Give the extent of all Plasmodium falciparum-infected red blood cells.
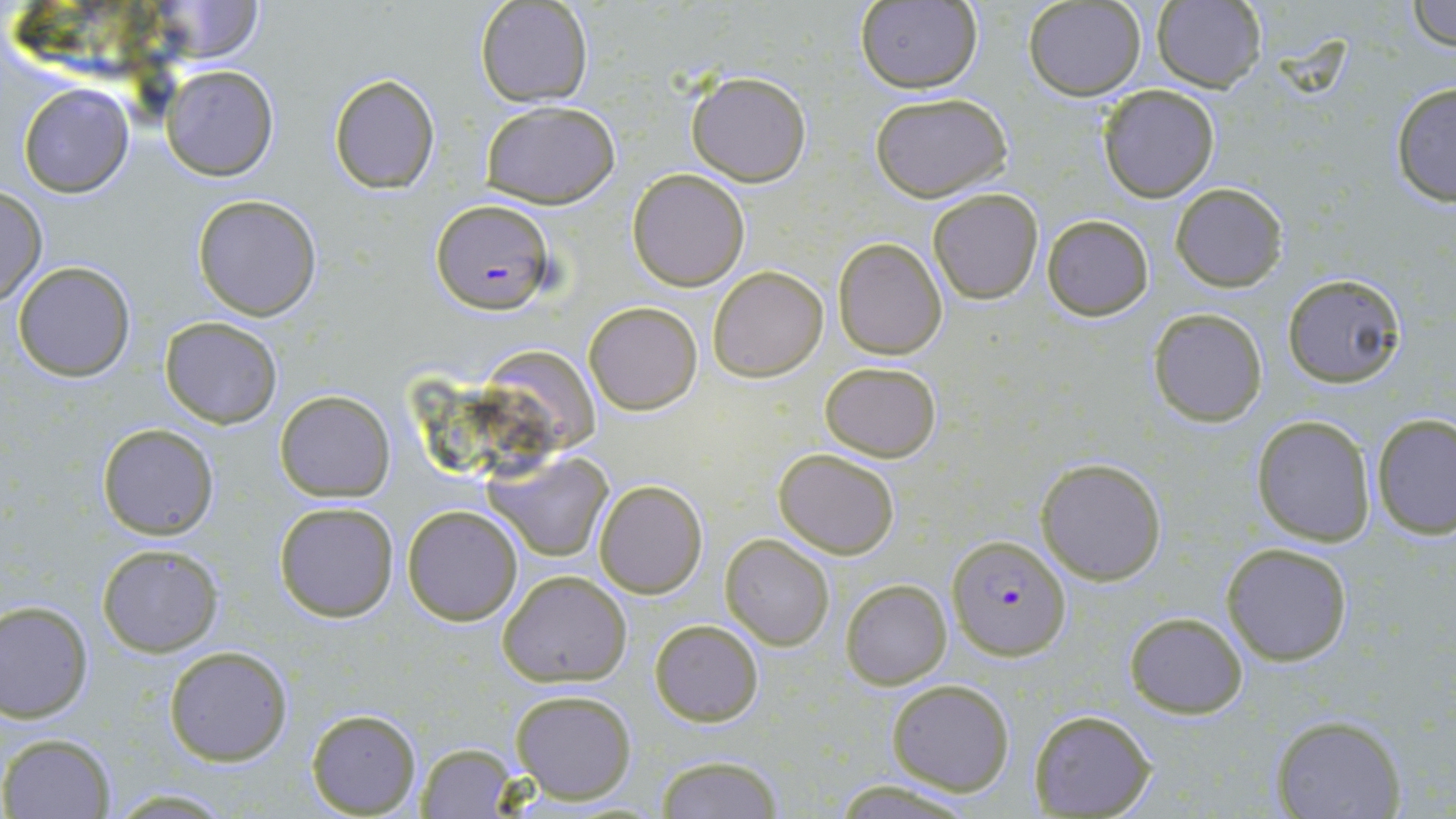
Approximate bounding boxes as [x1, y1, x2, y2] in pixels.
Plasmodium falciparum-infected red blood cells: [430, 197, 557, 314], [948, 534, 1070, 660].

slide_level_diagnosis: Plasmodium falciparum
magnification: 1000x
field_of_view: single
image_size: 1456×819 pixels
uninfected_red_blood_cell_locations: 'approximate bounding boxes as [x1, y1, x2, y2] in pixels: [1023, 0, 1146, 100], [1406, 0, 1456, 50], [474, 1, 593, 107], [854, 1, 982, 93], [1153, 1, 1267, 93], [151, 2, 266, 64], [163, 64, 280, 182], [685, 70, 813, 187], [327, 71, 441, 195], [1389, 79, 1456, 208], [18, 83, 135, 197], [1096, 83, 1221, 202], [869, 91, 1013, 203], [480, 100, 620, 207], [626, 168, 750, 292], [1170, 182, 1287, 291], [0, 186, 47, 309], [927, 187, 1044, 305], [191, 193, 324, 321], [1040, 213, 1155, 321], [834, 239, 947, 359], [12, 261, 136, 382], [708, 265, 829, 382], [1281, 272, 1406, 388], [585, 301, 703, 415], [1148, 307, 1268, 427], [160, 317, 282, 428], [479, 344, 606, 451], [820, 361, 941, 462], [275, 389, 395, 501], [1372, 413, 1455, 537], [1251, 415, 1376, 547], [97, 423, 219, 539], [774, 448, 899, 559], [489, 451, 614, 561], [1035, 456, 1168, 585], [593, 479, 707, 599], [273, 500, 399, 622], [402, 504, 524, 626], [719, 534, 834, 652], [96, 541, 225, 657], [1221, 541, 1353, 665], [497, 569, 632, 687], [842, 579, 951, 689], [0, 601, 95, 722], [1123, 611, 1249, 718], [648, 617, 764, 727], [163, 644, 293, 767], [886, 678, 1015, 795], [509, 688, 637, 803], [307, 708, 421, 816], [1029, 709, 1155, 816], [1269, 714, 1407, 819], [2, 733, 114, 817], [414, 742, 519, 817], [652, 755, 788, 818], [831, 780, 978, 817], [108, 789, 237, 817]'
modality: light microscopy
preparation: thin blood smear
stain: May-Grünwald-Giemsa